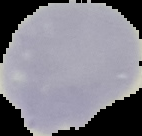

preparation = thin blood film
result = no Plasmodium parasites seen
image size = 142×136 pixels
image type = segmented cell region on a black background